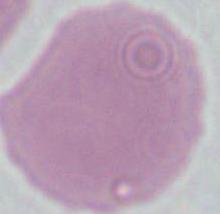
Photomicrograph. An erythrocyte is seen. Captured at 1000x magnification.